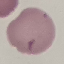

result = no malaria parasites detected
preparation = thin blood film
stain = Giemsa
image type = automatically extracted cell patch, resized to 64 × 64 pixels
capture = smartphone through the microscope eyepiece